Locate platelets.
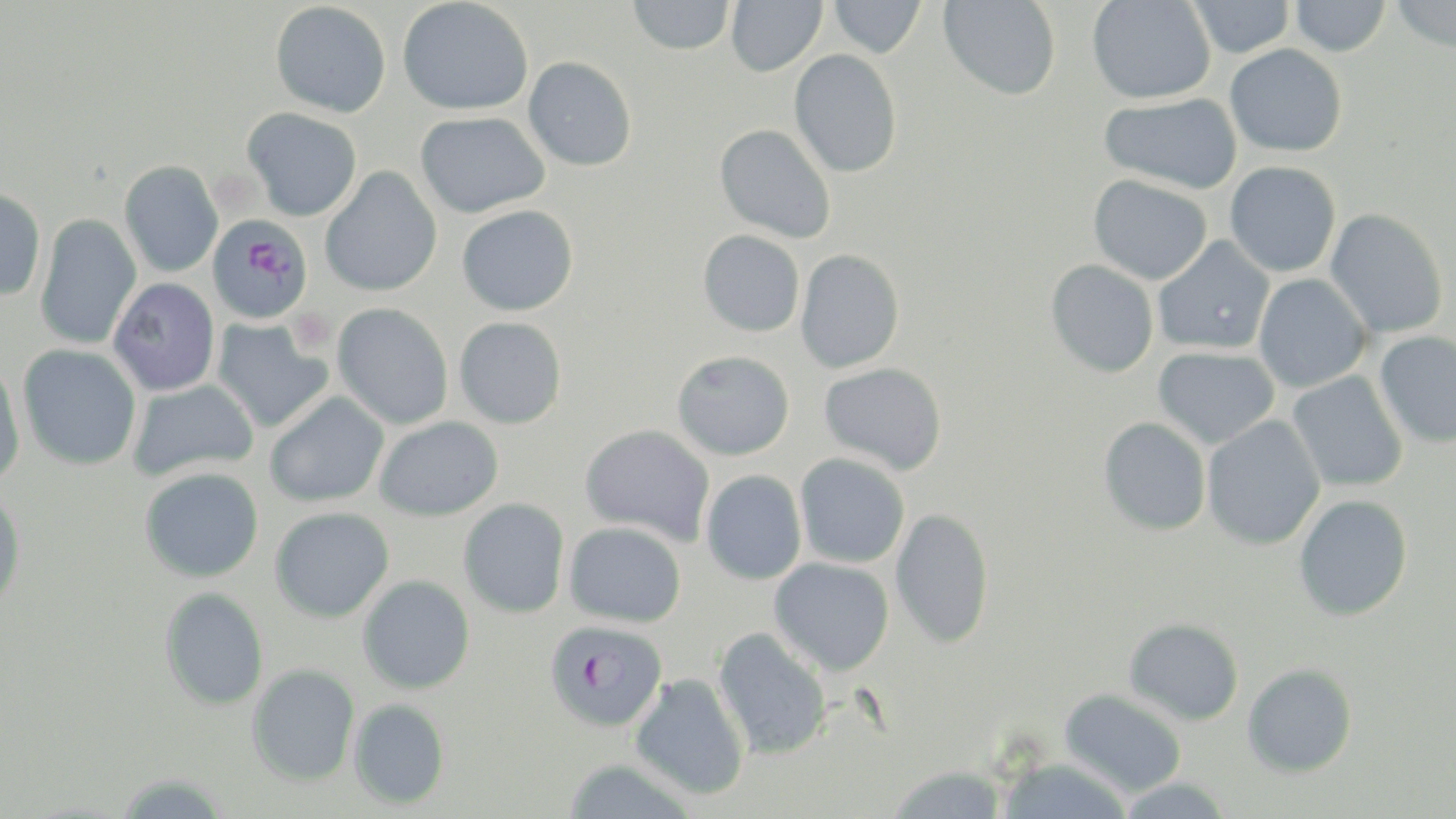

Approximate bounding boxes as [x1, y1, x2, y2] in pixels.
Platelets: [288, 308, 335, 355].

slide-level diagnosis = Plasmodium falciparum
field of view = one of a larger specimen
stain = May-Grünwald-Giemsa
Plasmodium falciparum-infected red blood cell locations = approximate bounding boxes as [x1, y1, x2, y2] in pixels: [210, 213, 317, 323], [544, 620, 668, 731]
magnification = 1000x
uninfected red blood cell locations = approximate bounding boxes as [x1, y1, x2, y2] in pixels: [398, 0, 534, 115], [627, 0, 735, 55], [725, 0, 827, 76], [828, 0, 927, 58], [938, 0, 1061, 100], [1087, 0, 1215, 104], [1390, 0, 1456, 54], [270, 1, 391, 117], [1187, 1, 1295, 58], [1290, 1, 1392, 57], [1225, 44, 1347, 156], [789, 50, 902, 178], [523, 56, 637, 170], [1099, 93, 1242, 194], [242, 107, 362, 221], [416, 111, 549, 217], [714, 124, 836, 243], [119, 161, 223, 277], [1225, 161, 1341, 277], [320, 166, 442, 297], [1088, 175, 1212, 284], [0, 188, 46, 301], [457, 204, 578, 315], [1326, 208, 1449, 338], [35, 213, 142, 350], [697, 229, 805, 337], [1153, 236, 1275, 355], [795, 249, 905, 373], [1045, 259, 1159, 378], [1253, 273, 1371, 392], [108, 278, 220, 396], [332, 303, 453, 429], [454, 316, 567, 429], [210, 319, 332, 434], [1375, 331, 1456, 447], [18, 344, 141, 471], [1153, 346, 1279, 449], [672, 350, 794, 460], [0, 360, 26, 489], [819, 362, 947, 475], [1287, 372, 1408, 492], [128, 379, 259, 480], [264, 392, 389, 508], [375, 416, 503, 521], [1202, 416, 1326, 550], [1098, 417, 1211, 536], [580, 424, 716, 546], [795, 453, 910, 568], [139, 467, 264, 582], [700, 470, 807, 585], [0, 486, 26, 613], [1293, 494, 1413, 622], [458, 499, 570, 618], [270, 507, 394, 623], [890, 508, 994, 649], [565, 521, 686, 628], [769, 558, 895, 674], [357, 575, 475, 694], [159, 587, 268, 711], [1124, 617, 1244, 725], [713, 627, 832, 760], [1242, 663, 1358, 777], [246, 664, 360, 786], [629, 674, 749, 800], [1059, 689, 1187, 796], [349, 698, 450, 810], [996, 757, 1134, 819], [561, 760, 697, 819], [885, 764, 1009, 818], [110, 773, 234, 817], [1115, 775, 1235, 818]
preparation = thin blood smear
image size = 1456×819 pixels
modality = optical microscopy